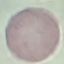
result = negative for malaria parasites
image type = cell patch, automatically extracted from a larger field of view and resized to 64 × 64 pixels
preparation = thin blood smear
stain = Giemsa
capture = smartphone through the microscope eyepiece